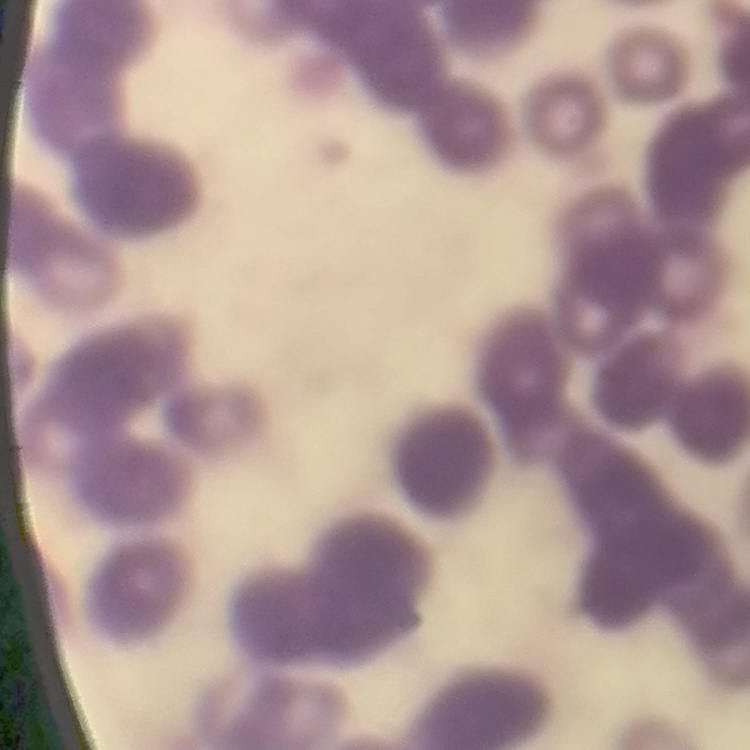
red blood cell morphology = rouleaux formation
preparation = thin blood smear
stain = Field's or Giemsa
image type = one tile cut from a larger photomicrograph